Report the malaria status of this cell.
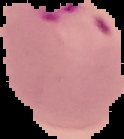
It is parasitized.

Summary:
  - Preparation: thin blood smear
  - Image type: segmented cell region with the area outside set to black
  - Image size: 124×139 pixels